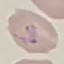

malaria status = parasitized
capture = smartphone camera at the microscope eyepiece
preparation = thin blood film
image type = cell patch, automatically extracted from a larger field of view and resized to 64 × 64 pixels
stain = Giemsa